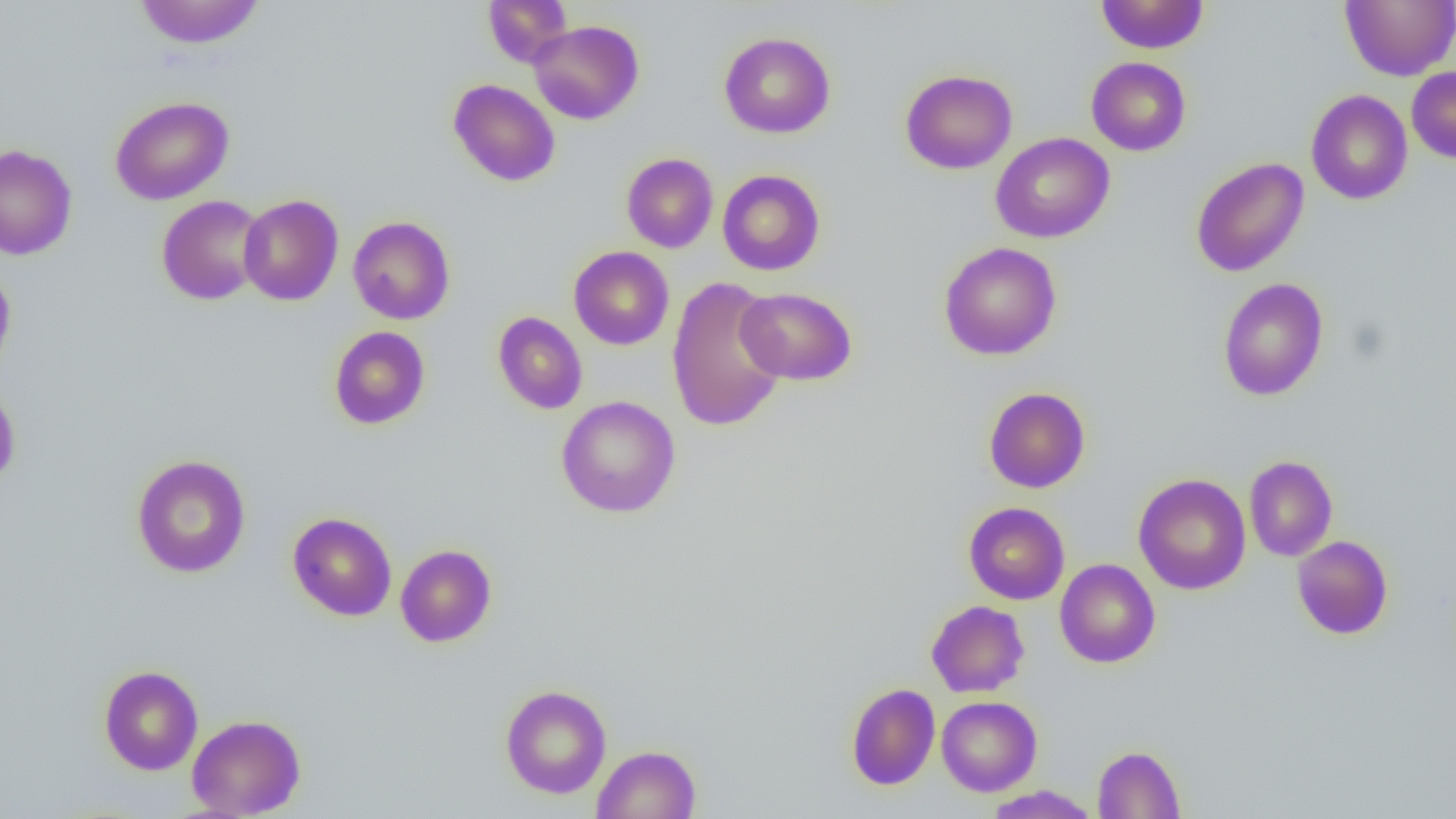 Approximate bounding boxes as (x1,y1)-(x2,y2) corner pairs in pixels. Uninfected red blood cell locations: (133,0)-(265,49), (483,0)-(573,68), (1095,0)-(1209,54), (1340,0)-(1456,81), (529,20)-(644,125), (719,32)-(835,138), (1086,56)-(1191,156), (1407,67)-(1456,163), (900,69)-(1017,174), (448,79)-(560,186), (1306,89)-(1412,205), (110,95)-(234,205), (990,133)-(1115,243), (0,144)-(77,260), (621,153)-(718,253), (1191,157)-(1309,277), (717,169)-(825,275), (156,195)-(267,305), (238,195)-(343,306), (348,216)-(455,324), (939,241)-(1062,360), (569,246)-(674,350), (0,261)-(16,378), (667,277)-(788,433), (1217,277)-(1329,401), (736,287)-(856,385), (493,311)-(587,414), (329,326)-(430,430), (0,382)-(20,488), (983,387)-(1090,493), (556,395)-(681,518), (131,454)-(251,578), (1243,455)-(1338,562), (1133,473)-(1251,595), (964,502)-(1070,605), (287,512)-(397,621), (1292,535)-(1393,639), (395,544)-(497,647), (1055,559)-(1160,668), (926,600)-(1029,698), (98,665)-(203,775), (846,683)-(940,790), (500,684)-(612,798), (936,695)-(1042,796), (187,714)-(306,818), (592,744)-(701,818), (1093,745)-(1185,818), (984,785)-(1099,818). Slide-level diagnosis: no evidence of blood parasites. Thin blood smear. Image is 1456×819 pixels. One field of a larger specimen. Captured at 1000x magnification. Optical microscopy.